Assess this cell for malaria.
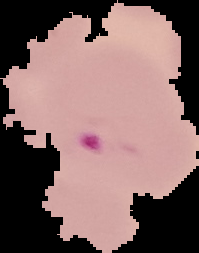
Parasitized.

Summary:
  - Image type: cell region segmented out of the field of view; surrounding area masked to black
  - Image size: 199×253 pixels
  - Preparation: thin blood film